Report the malaria status of this cell.
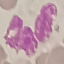
Uninfected.

Summary:
  - Image type: cell patch, automatically extracted from a larger field of view and resized to 64 × 64 pixels
  - Stain: Giemsa
  - Capture: smartphone camera at the microscope eyepiece
  - Preparation: thin smear